State which parasite is depicted.
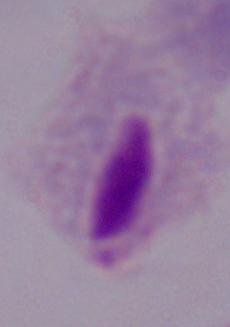

A trichomonad.

Summary:
  - Magnification: 1000x
  - Modality: photomicrograph